Name the blood parasite species.
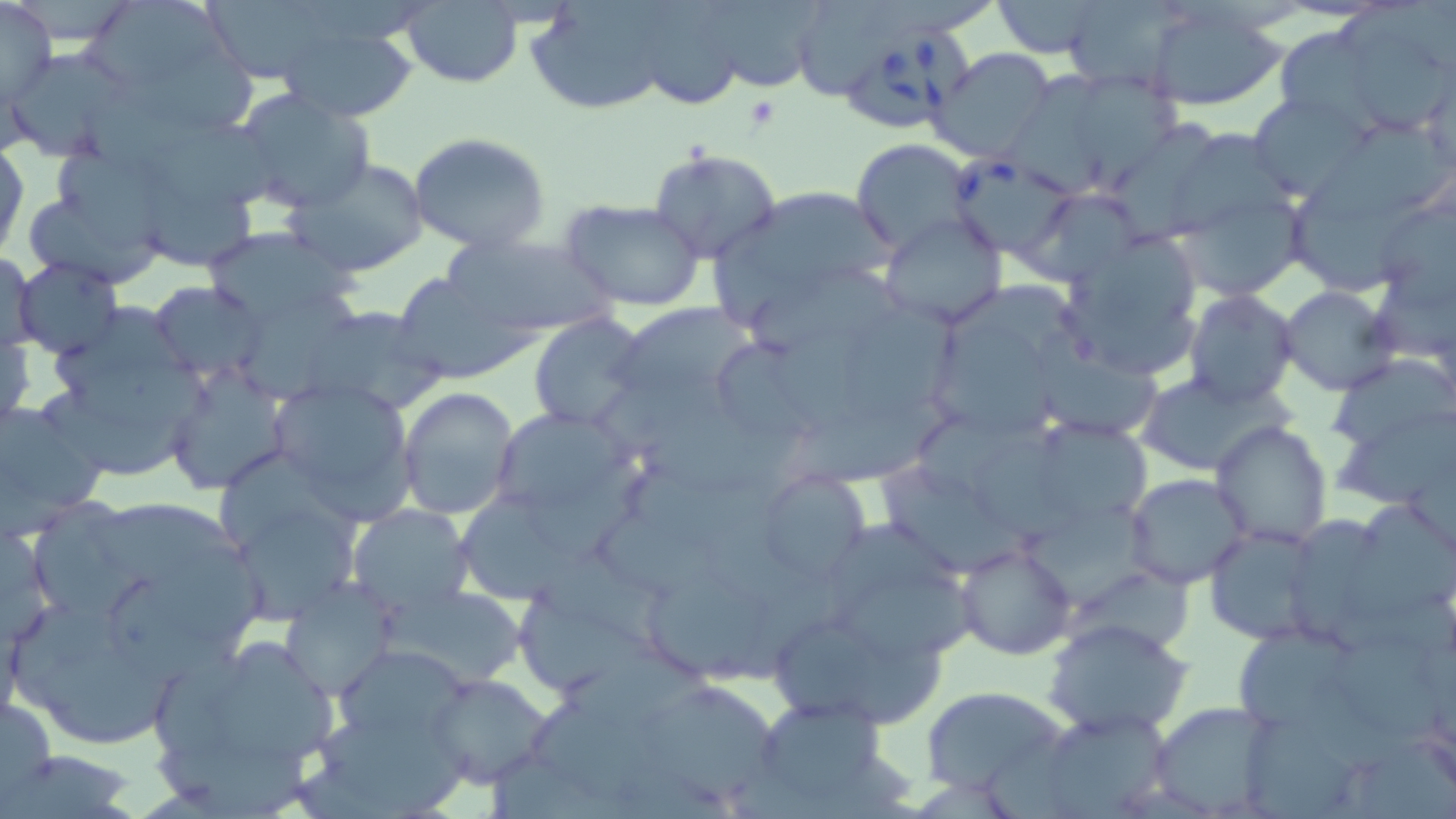
Babesia divergens.

Approximate bounding boxes as (x1,y1)-(x2,y2) corner pairs in pixels. Platelet locations: (743,96)-(779,129). Babesia divergens-infected red blood cell locations: (822,26)-(969,137), (949,155)-(1077,257). Uninfected red blood cell locations: (200,0)-(335,83), (526,0)-(683,116), (624,0)-(753,112), (0,1)-(57,109), (993,1)-(1109,57), (401,2)-(522,87), (1148,2)-(1288,111), (689,4)-(827,96), (85,5)-(235,92), (275,20)-(420,123), (1279,25)-(1379,125), (1351,33)-(1454,137), (930,47)-(1058,164), (2,50)-(129,159), (1036,65)-(1186,188), (231,90)-(375,214), (1249,93)-(1371,198), (1307,123)-(1449,229), (55,131)-(174,250), (406,132)-(555,256), (851,140)-(975,254), (649,147)-(781,265), (0,149)-(27,259), (287,161)-(429,280), (701,181)-(900,332), (1282,187)-(1440,297), (1026,188)-(1142,284), (1180,188)-(1308,302), (562,198)-(707,312), (879,213)-(1006,331), (200,228)-(360,333), (1057,230)-(1207,377), (437,232)-(622,341), (3,255)-(43,356), (13,260)-(123,357), (387,272)-(535,386), (148,280)-(264,381), (1279,286)-(1396,396), (1186,290)-(1298,409), (611,302)-(759,411), (298,304)-(446,417), (526,312)-(650,433), (40,314)-(212,483), (1,321)-(35,431), (928,322)-(1063,440), (1330,353)-(1455,453), (163,364)-(289,494), (1132,370)-(1291,476), (269,380)-(420,517), (398,387)-(521,520), (0,396)-(110,537), (488,404)-(636,522), (1211,420)-(1332,547), (1045,421)-(1156,523), (880,465)-(1031,582), (755,470)-(872,587), (1124,474)-(1251,589), (30,496)-(153,614), (462,496)-(596,608), (100,499)-(244,580), (348,505)-(474,619), (1338,505)-(1455,632), (1204,525)-(1321,642), (954,541)-(1076,660), (148,548)-(274,647), (647,576)-(772,682), (832,576)-(992,668), (279,579)-(399,701), (386,583)-(529,689), (772,611)-(894,723), (1044,617)-(1192,739), (1230,626)-(1362,738), (1334,626)-(1451,749), (149,628)-(343,803), (335,643)-(473,744), (38,647)-(173,739), (427,673)-(557,790), (637,679)-(781,810), (920,685)-(1070,799), (0,693)-(56,813), (743,693)-(901,816), (1151,701)-(1278,816), (1033,709)-(1174,815). 1000x magnification. Light microscopy. Image is 1456×819 pixels. Single field of view. Thin blood film. May-Grünwald-Giemsa stain.